Identify the parasite.
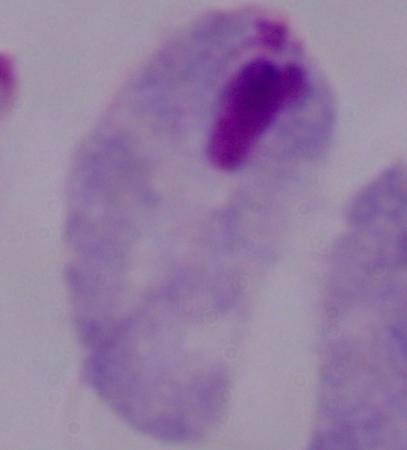
A trichomonad.

Summary:
  - Modality: micrograph
  - Magnification: 1000x